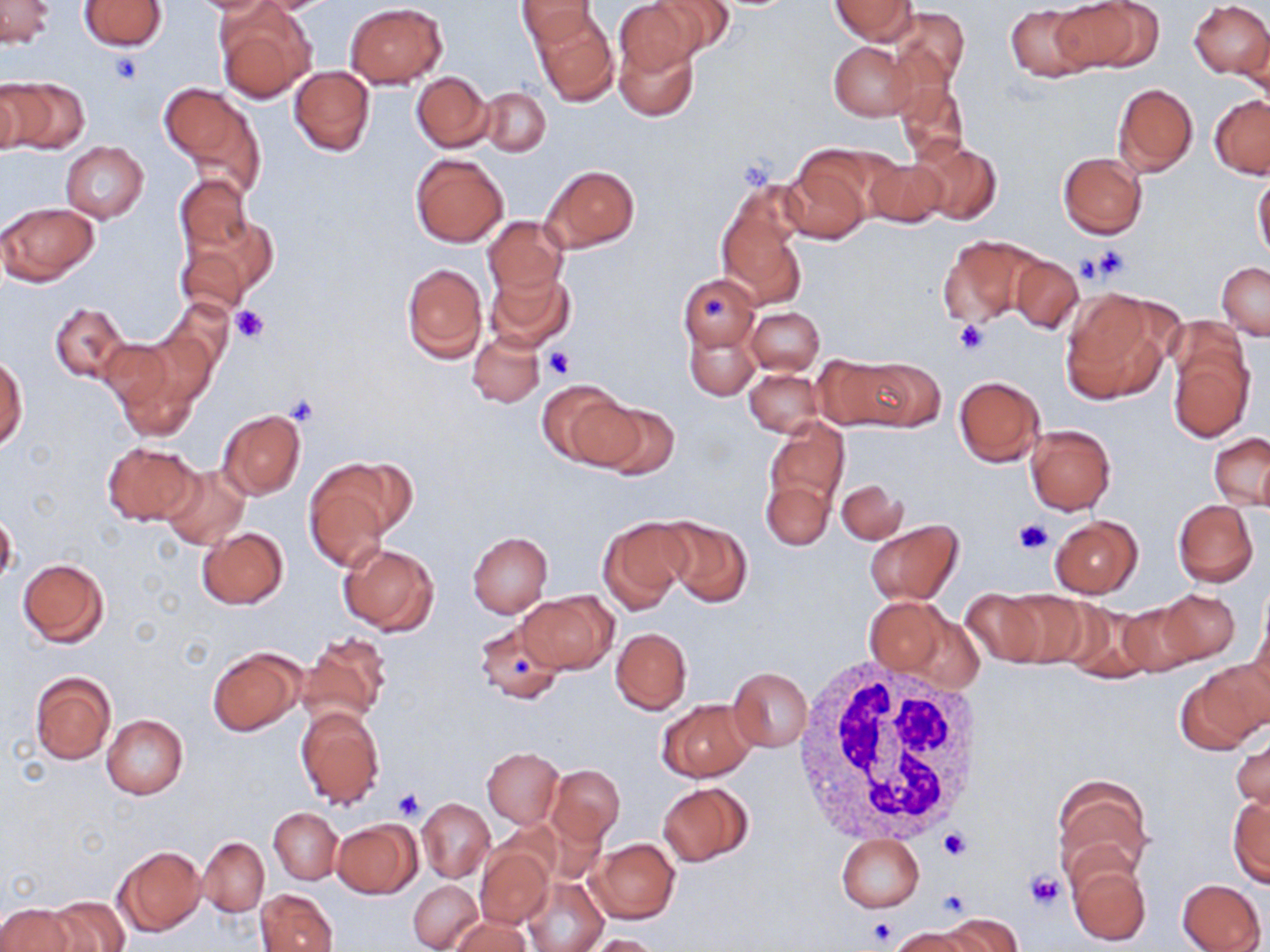
Summary:
  - Coordinate format: approximate bounding boxes as (x1, y1, x2, y2) in pixels
  - Platelet locations: (109, 55, 142, 84), (1083, 244, 1134, 285), (1076, 253, 1109, 284), (698, 293, 733, 320), (230, 305, 270, 344), (954, 318, 989, 356), (543, 346, 574, 379), (284, 394, 320, 427), (1014, 518, 1054, 554), (511, 655, 532, 677), (394, 788, 425, 820), (938, 825, 972, 861), (1026, 871, 1064, 907), (935, 888, 973, 920), (866, 917, 898, 946)
  - Uninfected red blood cell locations: (80, 0, 166, 50), (186, 0, 281, 15), (518, 0, 598, 48), (614, 0, 702, 75), (653, 0, 734, 58), (833, 0, 916, 43), (1048, 0, 1159, 73), (1189, 0, 1270, 79), (2, 1, 54, 47), (346, 2, 448, 88), (215, 3, 315, 102), (1005, 4, 1096, 81), (890, 6, 969, 92), (531, 9, 618, 106), (1240, 28, 1270, 105), (612, 38, 698, 121), (829, 41, 916, 120), (289, 65, 375, 156), (411, 71, 493, 152), (3, 77, 89, 155), (895, 81, 970, 165), (0, 83, 23, 156), (1113, 83, 1198, 176), (161, 85, 261, 190), (481, 86, 551, 156), (1209, 95, 1269, 178), (910, 141, 1001, 226), (61, 142, 149, 223), (410, 152, 508, 247), (781, 154, 872, 245), (1058, 154, 1147, 238), (862, 156, 948, 229), (543, 165, 638, 251), (1254, 172, 1270, 264), (172, 174, 253, 255), (716, 185, 806, 302), (1, 201, 100, 286), (482, 216, 568, 298), (178, 225, 273, 315), (938, 236, 1039, 327), (1009, 255, 1083, 332), (1218, 261, 1270, 339), (401, 263, 487, 363), (486, 267, 575, 352), (679, 273, 759, 353), (1060, 288, 1173, 404), (160, 298, 234, 380), (50, 303, 129, 382), (745, 307, 824, 374), (684, 327, 758, 401), (130, 330, 217, 422), (469, 332, 544, 407), (98, 336, 183, 422), (1167, 345, 1254, 442), (818, 353, 919, 430), (1, 356, 28, 450), (863, 357, 949, 433), (745, 368, 823, 436), (953, 374, 1045, 467), (536, 378, 629, 468), (590, 402, 681, 479), (217, 408, 306, 500), (765, 415, 849, 517), (1024, 424, 1116, 515), (1209, 434, 1269, 509), (102, 440, 201, 524), (161, 465, 250, 549), (304, 467, 393, 572), (760, 478, 834, 550), (837, 479, 906, 543), (1172, 500, 1258, 587), (0, 512, 17, 588), (598, 516, 689, 613), (1051, 516, 1142, 598), (659, 517, 752, 607), (865, 520, 963, 604), (197, 527, 289, 610), (468, 532, 552, 617), (339, 543, 439, 635), (17, 559, 109, 646), (959, 589, 1053, 668), (1157, 589, 1240, 664), (1000, 590, 1091, 669), (518, 592, 616, 673), (864, 597, 952, 676), (1054, 600, 1158, 681), (1114, 600, 1206, 677), (1249, 607, 1270, 699), (900, 611, 985, 694), (474, 620, 571, 704), (611, 628, 692, 713), (299, 631, 393, 727), (207, 648, 304, 736), (1180, 661, 1268, 753), (728, 666, 812, 752), (30, 671, 117, 764), (658, 698, 754, 782), (295, 706, 385, 810), (102, 715, 189, 800), (1232, 732, 1269, 812), (482, 748, 564, 827), (546, 764, 625, 846), (1051, 777, 1153, 883), (658, 782, 752, 865), (1228, 797, 1269, 887), (418, 798, 494, 881), (270, 808, 343, 883), (331, 821, 420, 898), (836, 834, 924, 912), (199, 837, 269, 915), (587, 838, 679, 923), (115, 846, 203, 935), (475, 847, 553, 929), (1066, 858, 1151, 947), (523, 876, 607, 952), (1177, 878, 1266, 952), (409, 880, 482, 951), (257, 889, 338, 952), (46, 896, 128, 952), (0, 904, 74, 952), (944, 912, 1023, 951), (450, 916, 528, 952), (890, 928, 979, 952), (589, 934, 664, 952)
  - White blood cell locations: (788, 655, 989, 844)
  - Slide-level diagnosis: negative for blood parasites
  - Preparation: thin blood film
  - Stain: May-Grünwald-Giemsa
  - Modality: optical microscopy
  - Image size: 1270×952 pixels
  - Field of view: single
  - Magnification: 1000x